Outline each Plasmodium vivax-infected red blood cell.
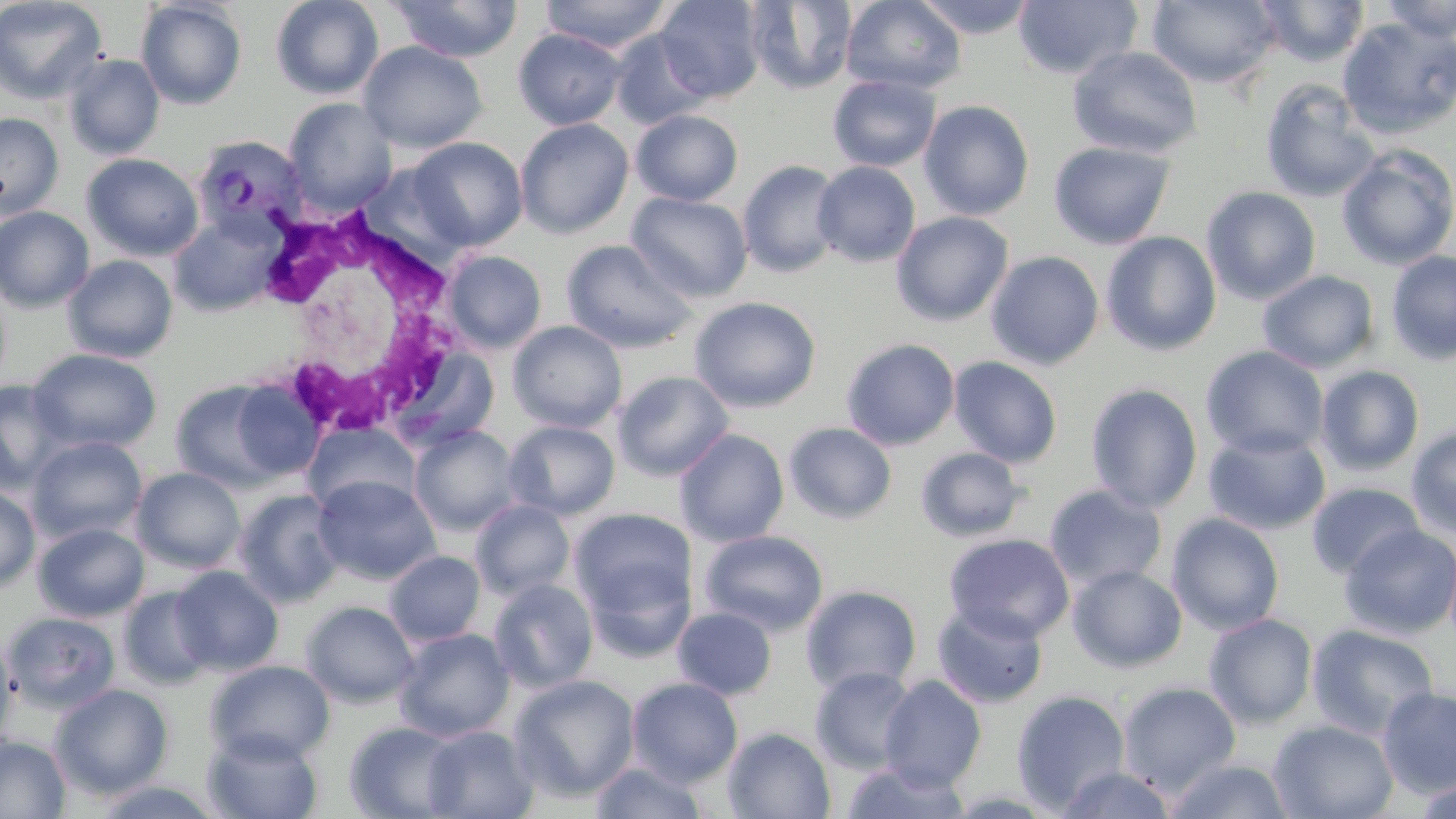
Approximate bounding boxes as (x1, y1, x2, y2) in pixels.
Plasmodium vivax-infected red blood cells: (192, 133, 309, 242).

White blood cell locations: (253, 204, 470, 445). Uninfected red blood cell locations: (0, 0, 107, 105), (270, 0, 384, 100), (389, 0, 522, 62), (539, 0, 675, 53), (654, 0, 766, 103), (841, 0, 967, 94), (912, 0, 1040, 38), (1013, 0, 1142, 80), (1146, 0, 1281, 89), (1254, 0, 1369, 67), (1377, 0, 1456, 43), (134, 1, 248, 110), (745, 1, 858, 94), (1338, 17, 1456, 139), (513, 28, 627, 130), (609, 28, 715, 129), (358, 41, 487, 153), (1067, 45, 1204, 159), (63, 53, 165, 159), (828, 74, 941, 172), (1259, 78, 1382, 203), (283, 97, 398, 214), (919, 99, 1035, 220), (631, 109, 744, 206), (0, 113, 64, 219), (515, 118, 634, 239), (407, 137, 528, 250), (1049, 140, 1175, 250), (1336, 145, 1456, 271), (81, 153, 204, 261), (738, 160, 843, 278), (812, 161, 921, 267), (1201, 186, 1321, 304), (627, 191, 753, 302), (0, 205, 95, 313), (891, 211, 1014, 326), (168, 213, 281, 317), (1101, 231, 1221, 356), (561, 239, 698, 352), (442, 250, 547, 353), (986, 250, 1104, 370), (1385, 250, 1456, 365), (62, 254, 179, 363), (1258, 270, 1380, 373), (689, 296, 822, 413), (507, 321, 627, 433), (841, 338, 960, 451), (389, 344, 502, 450), (1201, 346, 1329, 459), (27, 348, 162, 454), (948, 356, 1063, 468), (1315, 365, 1425, 476), (613, 370, 734, 481), (169, 378, 304, 493), (0, 379, 72, 493), (1085, 382, 1203, 513), (503, 420, 620, 520), (303, 422, 420, 515), (784, 422, 897, 524), (410, 425, 521, 535), (1406, 425, 1456, 539), (675, 429, 789, 547), (1202, 429, 1330, 535), (27, 436, 148, 544), (915, 447, 1028, 542), (132, 467, 245, 573), (313, 476, 441, 584), (1306, 482, 1424, 580), (0, 484, 41, 593), (1043, 484, 1168, 592), (233, 489, 346, 608), (470, 499, 575, 600), (571, 508, 694, 623), (1166, 513, 1285, 635), (32, 522, 149, 622), (1339, 523, 1456, 638), (699, 529, 828, 637), (944, 533, 1075, 643), (384, 550, 485, 646), (1067, 565, 1187, 673), (169, 566, 284, 675), (488, 578, 598, 692), (801, 585, 922, 695), (118, 586, 215, 690), (301, 601, 419, 708), (932, 603, 1048, 708), (672, 607, 777, 700), (2, 611, 121, 713), (1203, 613, 1318, 729), (1306, 624, 1439, 740), (393, 627, 514, 742), (0, 628, 19, 756), (206, 660, 335, 764), (810, 666, 919, 774), (509, 673, 640, 802), (879, 675, 986, 790), (627, 677, 743, 785), (1117, 682, 1242, 796), (51, 683, 173, 800), (1376, 687, 1456, 798), (1011, 690, 1131, 813), (1268, 720, 1398, 818), (345, 721, 463, 818), (421, 725, 539, 818), (722, 727, 836, 818), (202, 728, 324, 819), (0, 735, 70, 818), (1164, 758, 1295, 818), (589, 760, 708, 818), (839, 760, 971, 818), (1057, 766, 1178, 819), (1409, 775, 1455, 819), (85, 778, 229, 818). Slide-level diagnosis: Plasmodium vivax. Image is 1456×819 pixels. Single field of view. Thin blood film. 1000x magnification. May-Grünwald-Giemsa stain. Light microscopy.